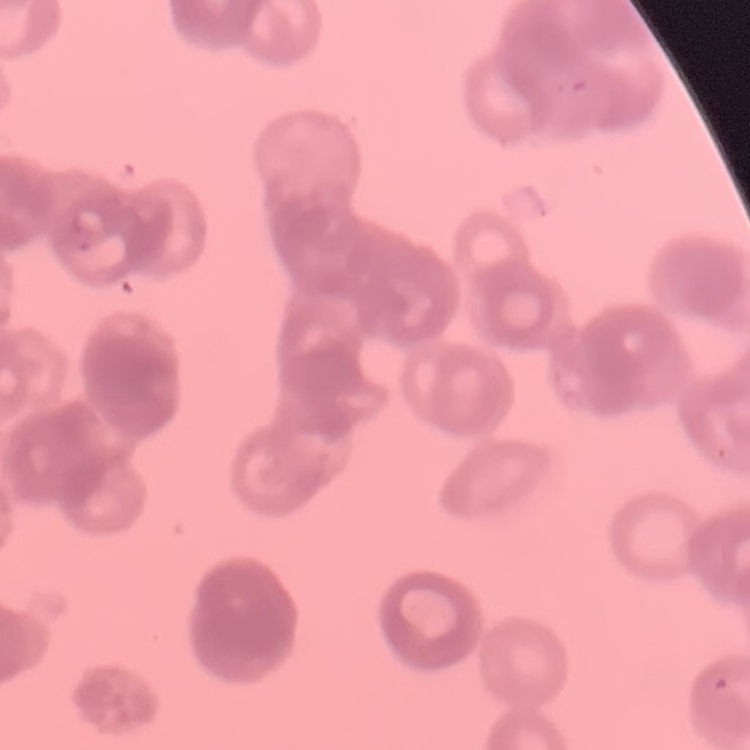
Summary:
  - Red blood cell morphology: rouleaux formation
  - Preparation: thin blood smear
  - Image type: one tile cut from a larger photomicrograph
  - Stain: Field's or Giemsa